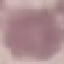
Summary:
  - Malaria status: uninfected
  - Stain: Giemsa
  - Image type: automatically extracted cell patch, resized to 64 × 64 pixels
  - Capture: smartphone through the microscope eyepiece
  - Preparation: thin smear